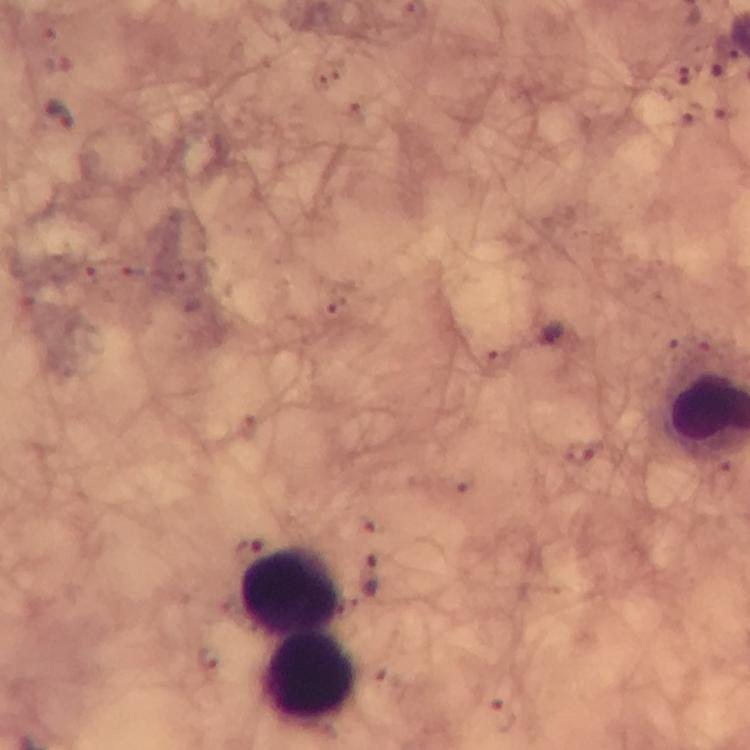

Approximate centers as (x, y) in pixels.
Summary:
  - Malaria parasite locations: (62, 115), (248, 547), (370, 573)
  - Leukocyte locations: (289, 588), (309, 681)
  - Image size: 750×750 pixels
  - Immersion oil: used
  - Cropped from: one field of view
  - Preparation: thick blood film
  - Context: from a malaria diagnostic workup
  - Capture: smartphone mounted on the microscope
  - Magnification: 100x
  - Stain: Giemsa